Describe the morphology of the red blood cells.
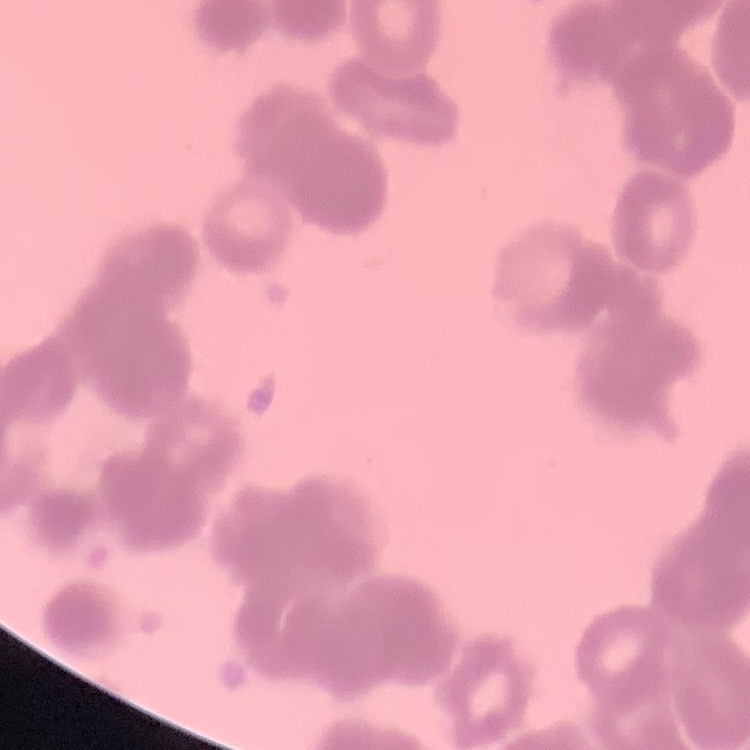

They show rouleaux formation.

Summary:
  - Image type: square crop of a larger photomicrograph
  - Preparation: thin peripheral smear
  - Stain: Field's or Giemsa